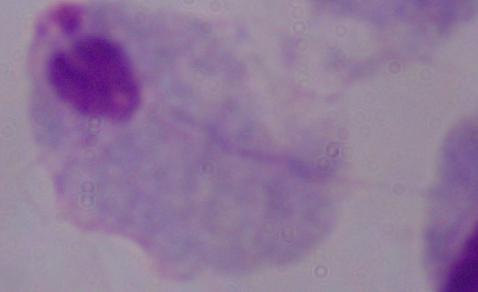 Micrograph. A trichomonad is seen. 1000x magnification.